Draw a bounding box around every leukocyte (white blood cell).
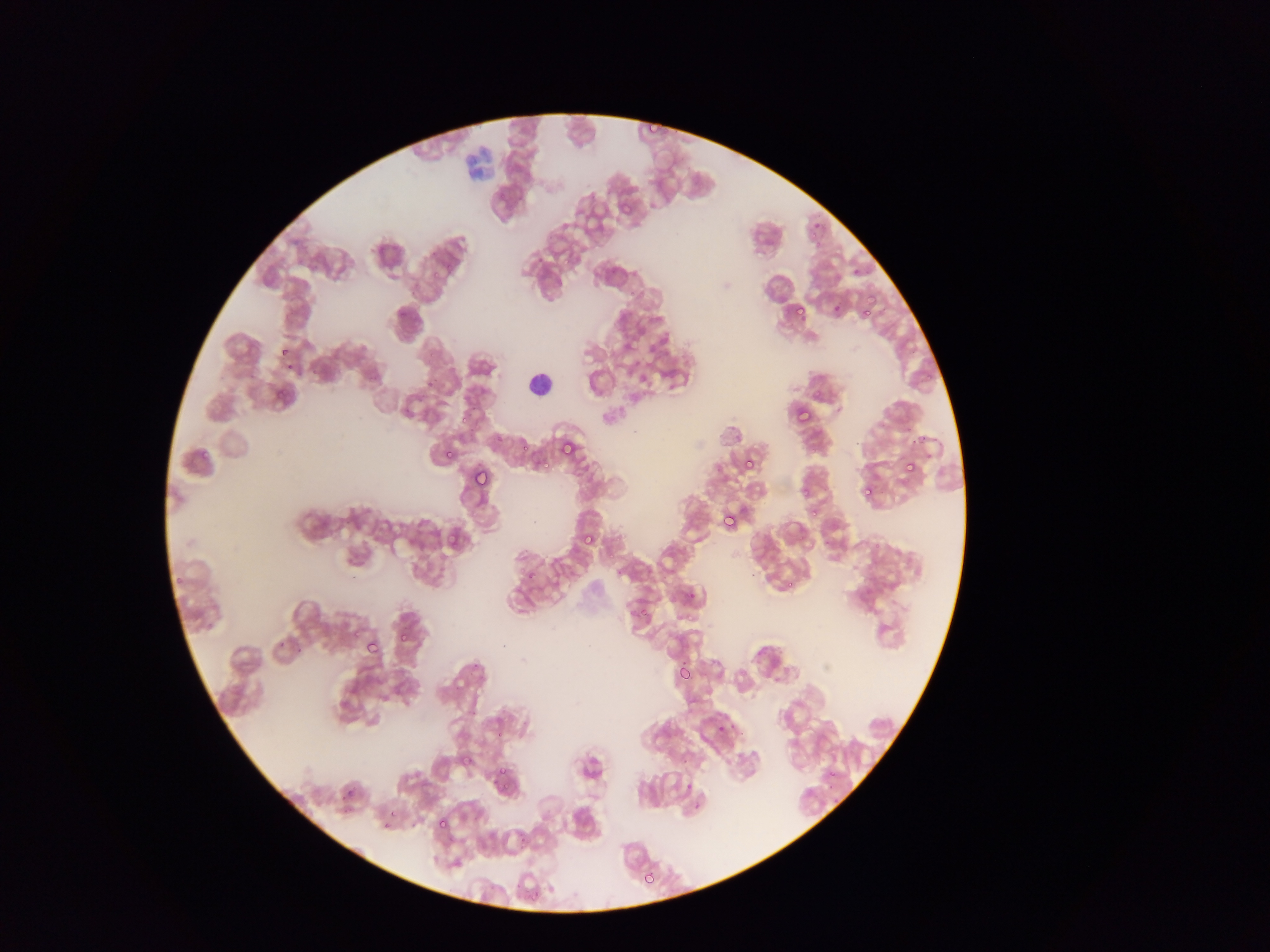
Approximate bounding boxes as {left, top, right, bottom} in pixels.
Leukocytes: {523, 368, 555, 399}.

country = Ghana
field of view = single
capture = mobile-phone photograph through a microscope
preparation = thin blood film
malaria parasite locations = approximate bounding boxes as {left, top, right, bottom} in pixels: {616, 199, 637, 220}, {849, 265, 864, 280}, {793, 303, 809, 321}, {862, 306, 874, 319}, {278, 343, 294, 362}, {272, 383, 292, 403}, {789, 397, 816, 424}, {490, 431, 506, 449}, {555, 438, 578, 463}, {534, 452, 553, 469}, {442, 453, 455, 460}, {743, 456, 760, 474}, {901, 457, 920, 478}, {472, 472, 490, 485}, {859, 488, 870, 500}, {804, 498, 822, 516}, {720, 508, 742, 530}, {440, 527, 465, 548}, {579, 529, 600, 551}, {682, 587, 700, 608}, {627, 601, 651, 625}, {395, 628, 412, 645}, {364, 638, 381, 657}, {675, 663, 695, 684}, {340, 682, 361, 705}, {715, 719, 732, 736}, {456, 751, 469, 773}, {492, 762, 513, 786}, {342, 784, 358, 802}, {434, 814, 453, 834}, {641, 868, 659, 889} | approximate {x, y} pixel centers of objects too small to bound: {523, 447}, {872, 481}
image size = 1270×952 pixels